Classify this cell by malaria status.
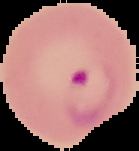

It is parasitized.

image size = 139×151 pixels
image type = cell region segmented out of the field of view; surrounding area masked to black
preparation = thin blood smear